Classify this cell by malaria status.
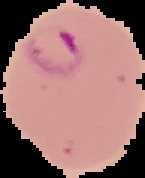
Parasitized.

image size = 145×178 pixels
image type = segmented cell region on a black background
preparation = thin blood smear